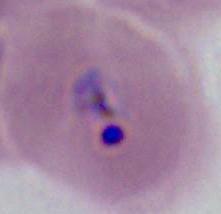
{
  "magnification": "400x or 1000x",
  "identification": "Plasmodium",
  "modality": "micrograph"
}